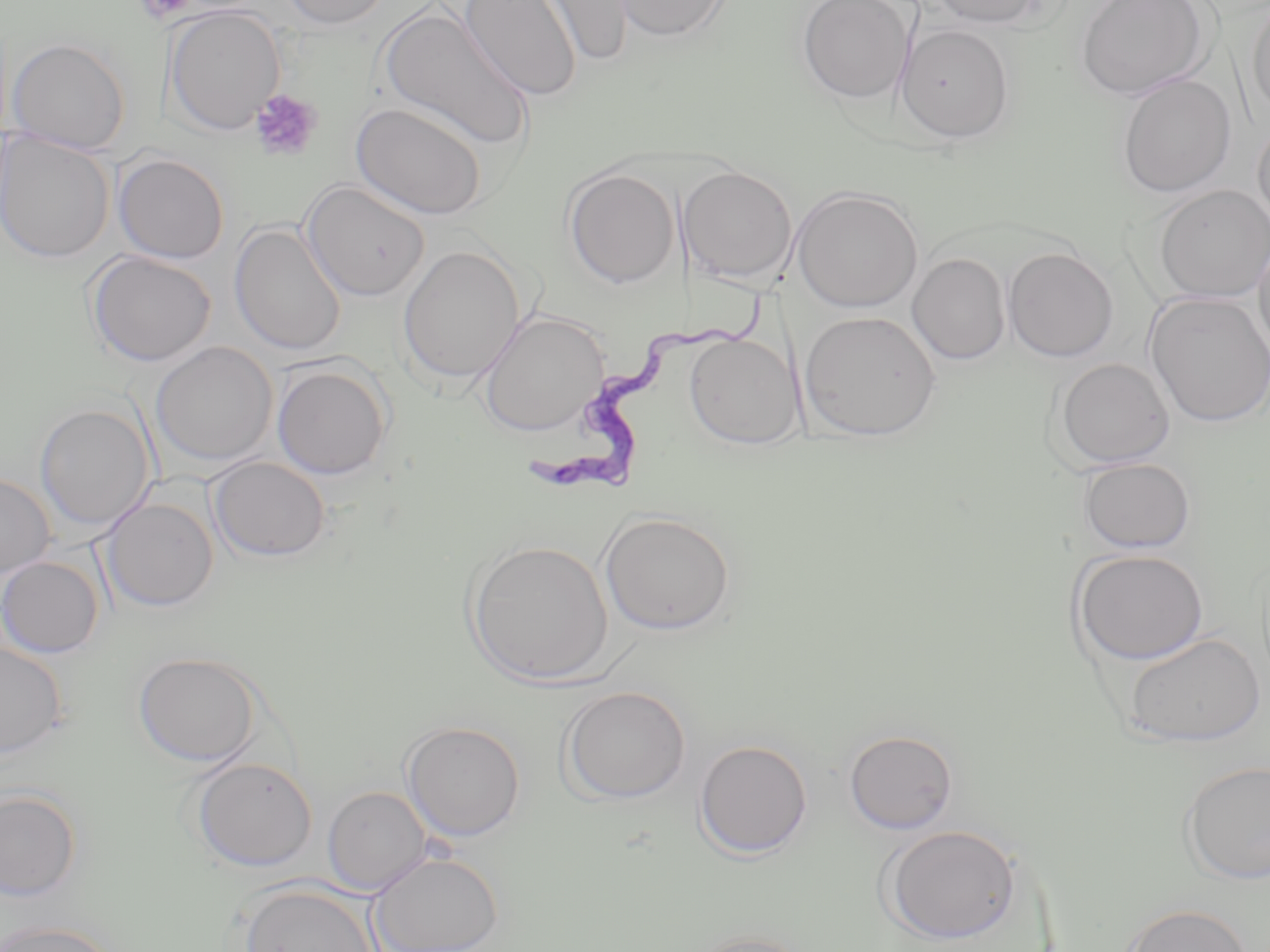

Approximate bounding boxes as [x1, y1, x2, y2] in pixels. Platelet locations: [133, 0, 200, 24], [250, 89, 324, 160]. Trypanosoma brucei locations: [523, 284, 781, 499]. Uninfected red blood cell locations: [277, 0, 395, 29], [460, 0, 581, 101], [535, 0, 636, 66], [609, 0, 731, 42], [797, 0, 915, 103], [928, 0, 1051, 28], [1075, 0, 1212, 101], [1247, 0, 1270, 122], [164, 6, 285, 136], [377, 6, 535, 153], [895, 24, 1014, 143], [7, 37, 131, 154], [1116, 74, 1236, 198], [351, 102, 488, 220], [1252, 118, 1270, 237], [0, 132, 115, 264], [112, 153, 230, 263], [679, 166, 798, 285], [563, 167, 680, 288], [301, 180, 430, 302], [1152, 184, 1270, 303], [791, 187, 924, 312], [229, 223, 346, 356], [1254, 232, 1270, 366], [397, 244, 526, 386], [1002, 247, 1119, 362], [86, 251, 216, 367], [907, 253, 1011, 365], [1144, 292, 1270, 427], [478, 310, 608, 436], [800, 310, 941, 441], [684, 333, 803, 449], [150, 342, 277, 467], [1053, 357, 1175, 469], [271, 361, 392, 480], [34, 403, 156, 532], [208, 456, 331, 562], [1078, 457, 1196, 554], [0, 473, 55, 577], [101, 496, 219, 613], [599, 511, 736, 636], [465, 538, 613, 687], [1071, 548, 1209, 665], [0, 555, 104, 658], [1123, 632, 1265, 747], [0, 641, 68, 759], [133, 651, 264, 767], [560, 686, 691, 805], [401, 720, 526, 842], [844, 729, 958, 834], [694, 739, 813, 859], [190, 757, 318, 872], [1179, 760, 1270, 886], [322, 786, 431, 895], [1, 788, 82, 901], [882, 824, 1024, 944], [369, 851, 504, 952], [236, 882, 382, 952], [1121, 903, 1253, 952], [1, 920, 120, 952], [682, 930, 815, 952]. Slide-level diagnosis: Trypanosoma brucei. Image is 1270×952 pixels. May-Grünwald-Giemsa-stained preparation. 1000x magnification. Single field of view. Thin blood smear. Optical microscopy.